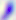
Summary:
  - Modality: micrograph
  - Magnification: 400x
  - Identification: Toxoplasma gondii